Assess this cell for malaria.
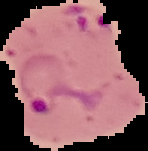
It is parasitized.

Image is 148×151 pixels. Segmented cell region on a black background. From a thin blood film.